Comment on the morphology of the red blood cells.
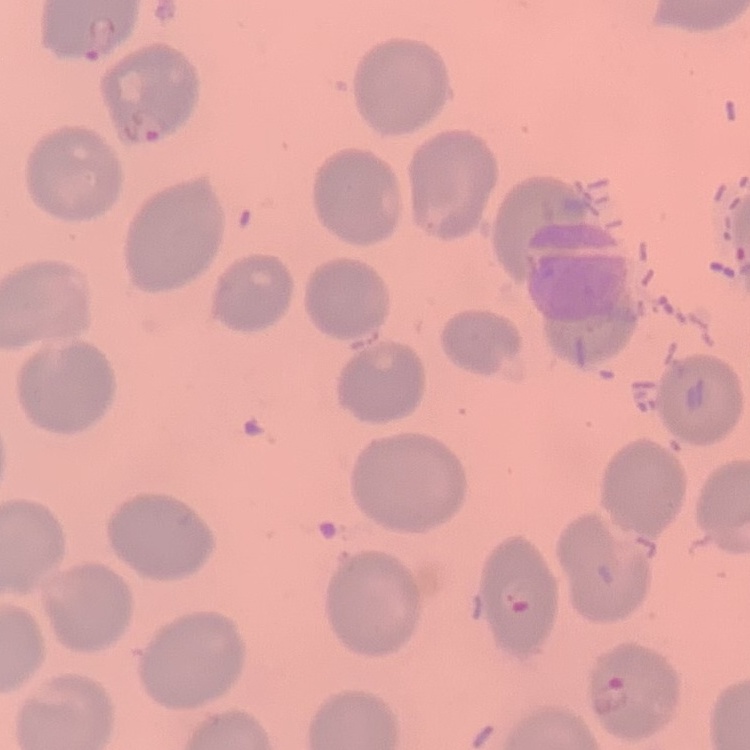

No rouleaux formation.

Thin blood smear. Stained with either Field's or Giemsa. Square crop of a larger photomicrograph.